State which cell type is depicted.
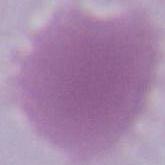
An erythrocyte.

Summary:
  - Modality: photomicrograph
  - Magnification: 1000x